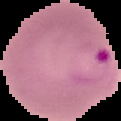
Summary:
  - Image size: 121×121 pixels
  - Preparation: thin blood film
  - Result: malaria parasites identified
  - Image type: segmented cell region with the area outside set to black